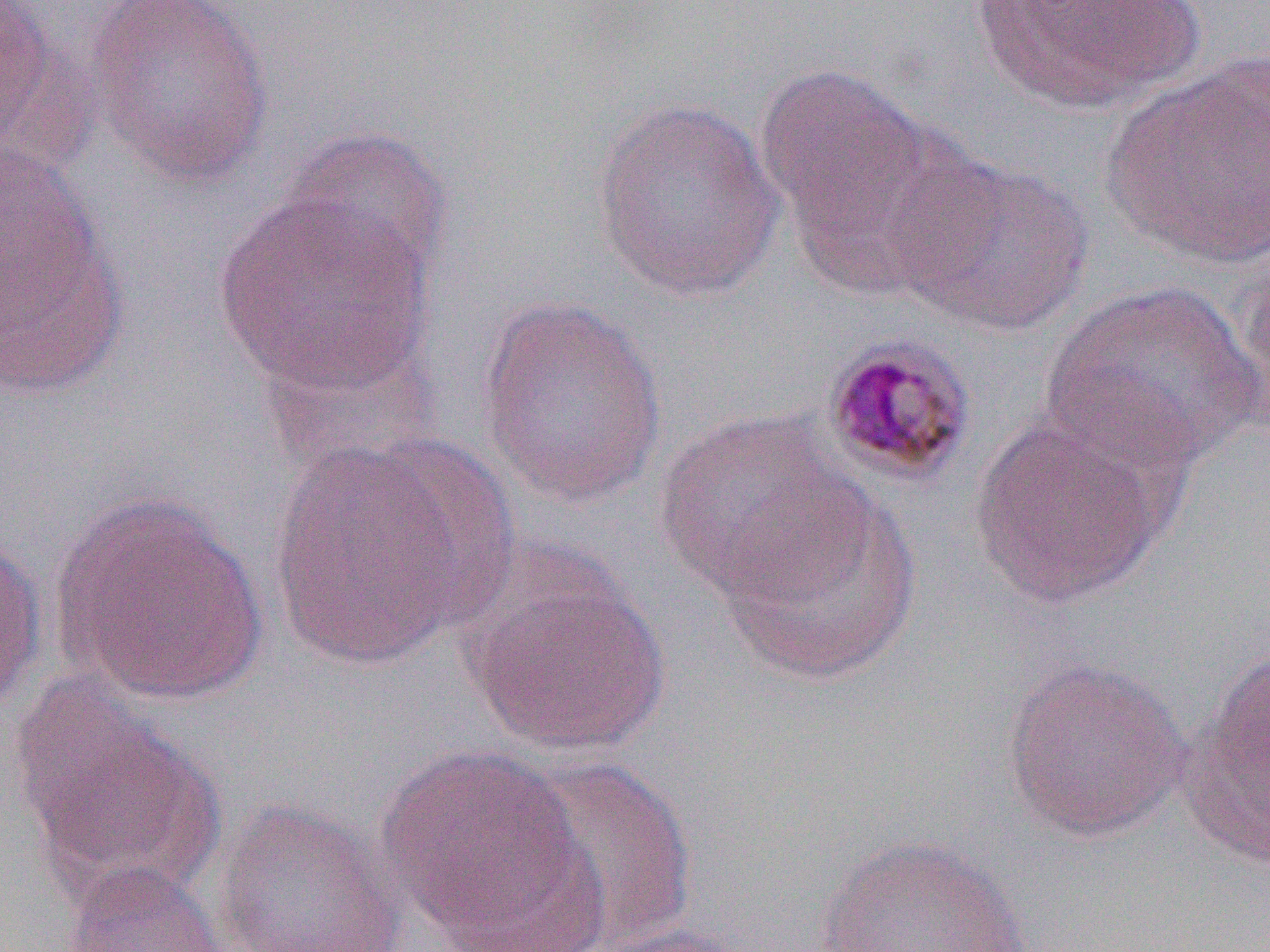

slide-level diagnosis = Plasmodium malariae
image size = 1270×952 pixels
preparation = thin blood film
magnification = 1000x
Plasmodium malariae-infected red blood cell locations = approximate bounding boxes as (x1, y1, x2, y2) in pixels: (820, 334, 978, 487)
field of view = single
modality = optical microscopy
uninfected red blood cell locations = approximate bounding boxes as (x1, y1, x2, y2) in pixels: (83, 0, 275, 187), (970, 0, 1202, 118), (1, 1, 60, 164), (1100, 57, 1270, 269), (756, 63, 943, 274), (589, 97, 785, 302), (279, 126, 455, 290), (891, 152, 1093, 337), (1, 162, 129, 402), (213, 188, 438, 401), (1233, 238, 1270, 439), (1039, 279, 1264, 473), (475, 292, 670, 511), (653, 411, 860, 598), (968, 412, 1172, 610), (267, 437, 485, 673), (713, 481, 922, 685), (53, 492, 269, 705), (0, 533, 47, 721), (462, 555, 671, 759), (1180, 648, 1270, 867), (1000, 657, 1191, 844), (12, 683, 222, 901), (375, 742, 595, 947), (514, 756, 698, 949), (211, 798, 410, 952), (814, 834, 1033, 952), (60, 860, 236, 952), (579, 922, 763, 952)